Report the malaria status of this cell.
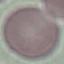
Uninfected.

Thin blood film. Cell patch, automatically extracted from a larger field of view and resized to 64 × 64 pixels. Giemsa-stained preparation. Acquired by smartphone through the microscope eyepiece.